Identify the parasite.
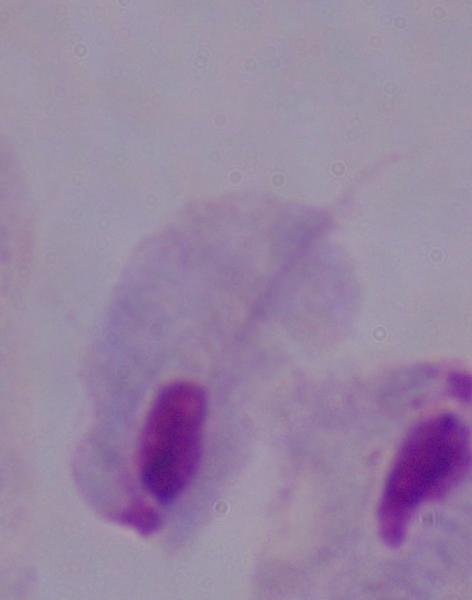

A trichomonad.

Captured at 1000x magnification. Micrograph.